Identify the parasite.
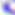
This is Toxoplasma gondii.

modality = micrograph
magnification = 400x